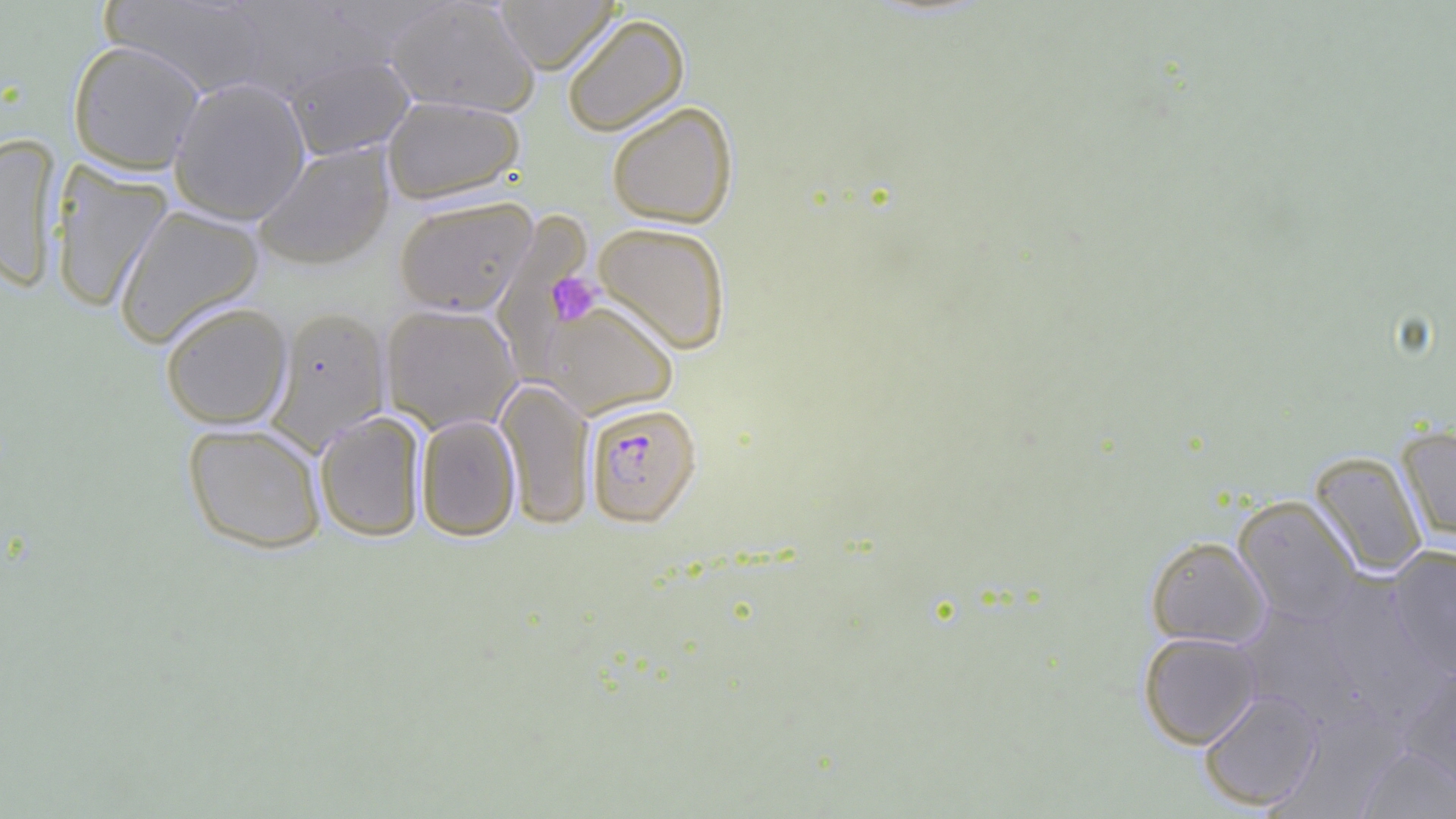
Approximate bounding boxes as (x1, y1, x2, y2) in pixels. Plasmodium falciparum-infected red blood cell locations: (584, 402, 702, 527). Uninfected red blood cell locations: (101, 0, 276, 98), (225, 0, 385, 101), (495, 0, 619, 73), (384, 1, 540, 117), (561, 13, 690, 137), (67, 40, 205, 174), (283, 53, 415, 160), (168, 77, 311, 225), (381, 96, 525, 205), (606, 101, 738, 229), (0, 134, 62, 293), (252, 141, 395, 271), (49, 161, 173, 313), (393, 195, 538, 316), (112, 204, 265, 348), (491, 213, 594, 377), (592, 221, 731, 355), (536, 299, 679, 418), (159, 301, 293, 429), (380, 303, 522, 434), (265, 305, 392, 454), (495, 379, 595, 529), (314, 410, 427, 542), (415, 414, 521, 541), (182, 422, 328, 554), (1397, 425, 1456, 544), (1309, 451, 1428, 579), (1232, 494, 1362, 627), (1146, 536, 1272, 650), (1387, 546, 1456, 681), (1318, 580, 1448, 727), (1235, 605, 1368, 732), (1138, 631, 1262, 749), (1400, 664, 1456, 793), (1199, 688, 1322, 811), (1357, 746, 1456, 818). Platelet locations: (523, 249, 605, 344), (544, 272, 602, 326). Slide-level diagnosis: Plasmodium falciparum. Image is 1456×819 pixels. Light microscopy. Single field of view. 1000x magnification. Thin blood smear.